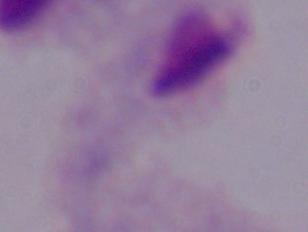
{
  "magnification": "1000x",
  "modality": "micrograph",
  "identification": "trichomonad"
}